Assess this cell for malaria.
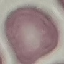
It is uninfected.

Summary:
  - Image type: automatically extracted cell patch, resized to 64 × 64 pixels
  - Capture: smartphone through the microscope eyepiece
  - Stain: Giemsa
  - Preparation: thin smear